Report the malaria status of this cell.
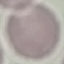
Uninfected.

Thin blood smear. Cell patch, automatically extracted from a larger field of view and resized to 64 × 64 pixels. Giemsa stain. Photographed with a smartphone camera at the microscope eyepiece.